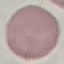
result: no malaria parasites seen
stain: Giemsa
capture: smartphone through the microscope eyepiece
image_type: automatically extracted cell patch, resized to 64 × 64 pixels
preparation: thin blood film